Give the extent of all Plasmodium malariae-infected red blood cells.
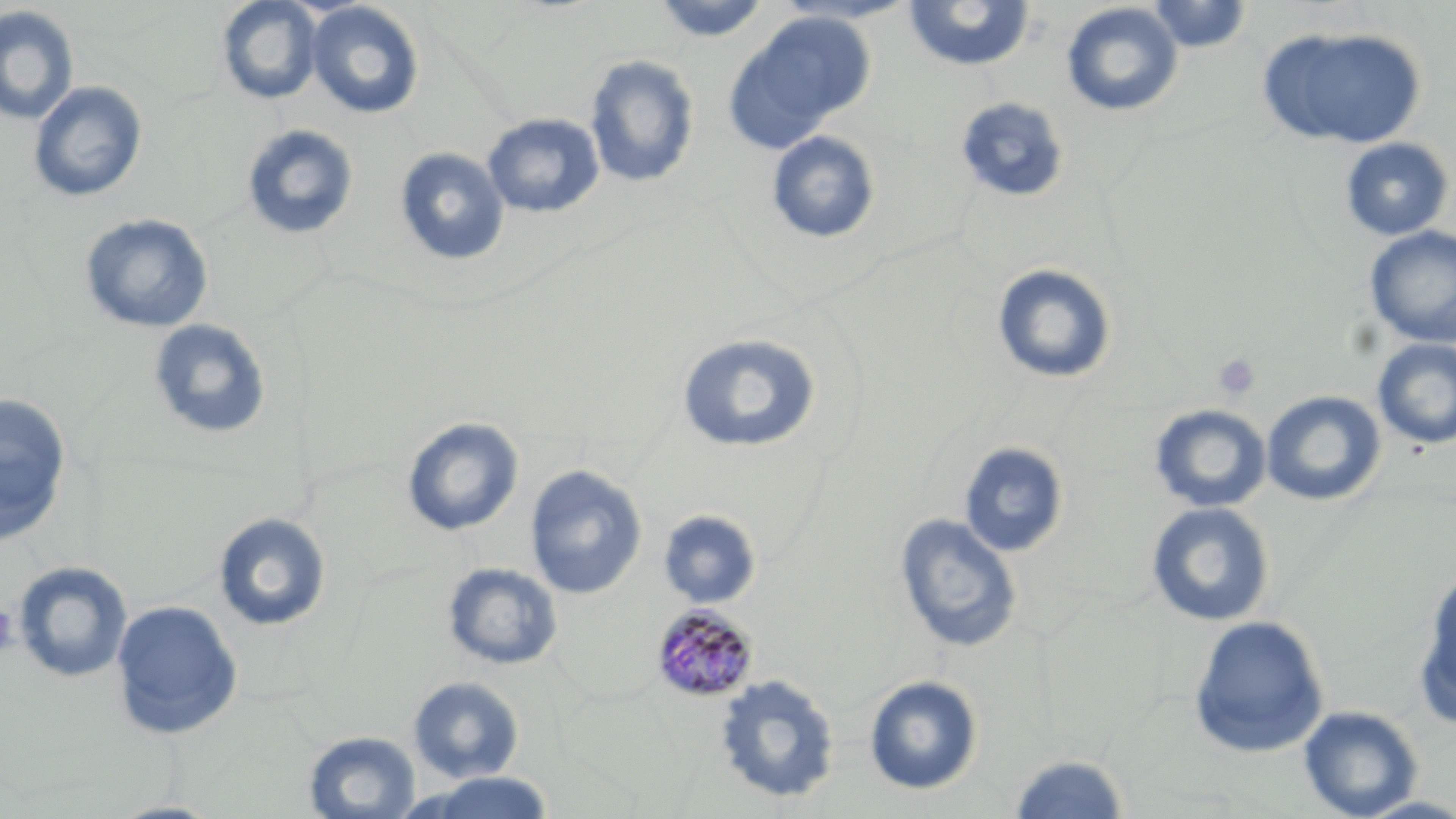
Approximate bounding boxes as (x1, y1, x2, y2) in pixels.
Plasmodium malariae-infected red blood cells: (650, 602, 759, 702).

Platelet locations: (1213, 353, 1260, 400), (0, 605, 19, 659). Uninfected red blood cell locations: (649, 0, 774, 43), (769, 0, 921, 25), (1145, 0, 1255, 53), (216, 1, 324, 105), (902, 1, 1036, 73), (306, 2, 425, 120), (1061, 2, 1184, 117), (0, 6, 79, 126), (723, 12, 875, 153), (1257, 25, 1426, 150), (584, 55, 700, 189), (28, 81, 148, 203), (954, 97, 1071, 204), (482, 113, 605, 219), (241, 124, 359, 240), (766, 130, 882, 245), (1339, 137, 1454, 241), (394, 147, 510, 267), (79, 213, 214, 333), (1363, 226, 1456, 347), (991, 262, 1118, 385), (148, 318, 272, 440), (676, 331, 823, 454), (1372, 339, 1456, 449), (1261, 390, 1387, 507), (0, 393, 72, 547), (1148, 404, 1272, 513), (401, 416, 525, 536), (957, 441, 1070, 558), (524, 465, 648, 599), (1146, 502, 1275, 627), (657, 509, 763, 610), (213, 512, 332, 631), (894, 513, 1022, 655), (13, 561, 133, 683), (442, 562, 564, 670), (1415, 566, 1456, 728), (111, 600, 244, 740), (1188, 615, 1329, 758), (713, 674, 841, 805), (863, 674, 984, 796), (408, 676, 526, 783), (1298, 705, 1424, 818), (303, 730, 421, 819), (1007, 753, 1132, 818), (405, 771, 558, 818), (106, 799, 228, 819). Slide-level diagnosis: Plasmodium malariae. Thin blood smear. Captured at 1000x magnification. Image is 1456×819 pixels. Optical microscopy. Single field of view. May-Grünwald-Giemsa-stained preparation.